Give the extent of all Plasmodium falciparum-infected red blood cells.
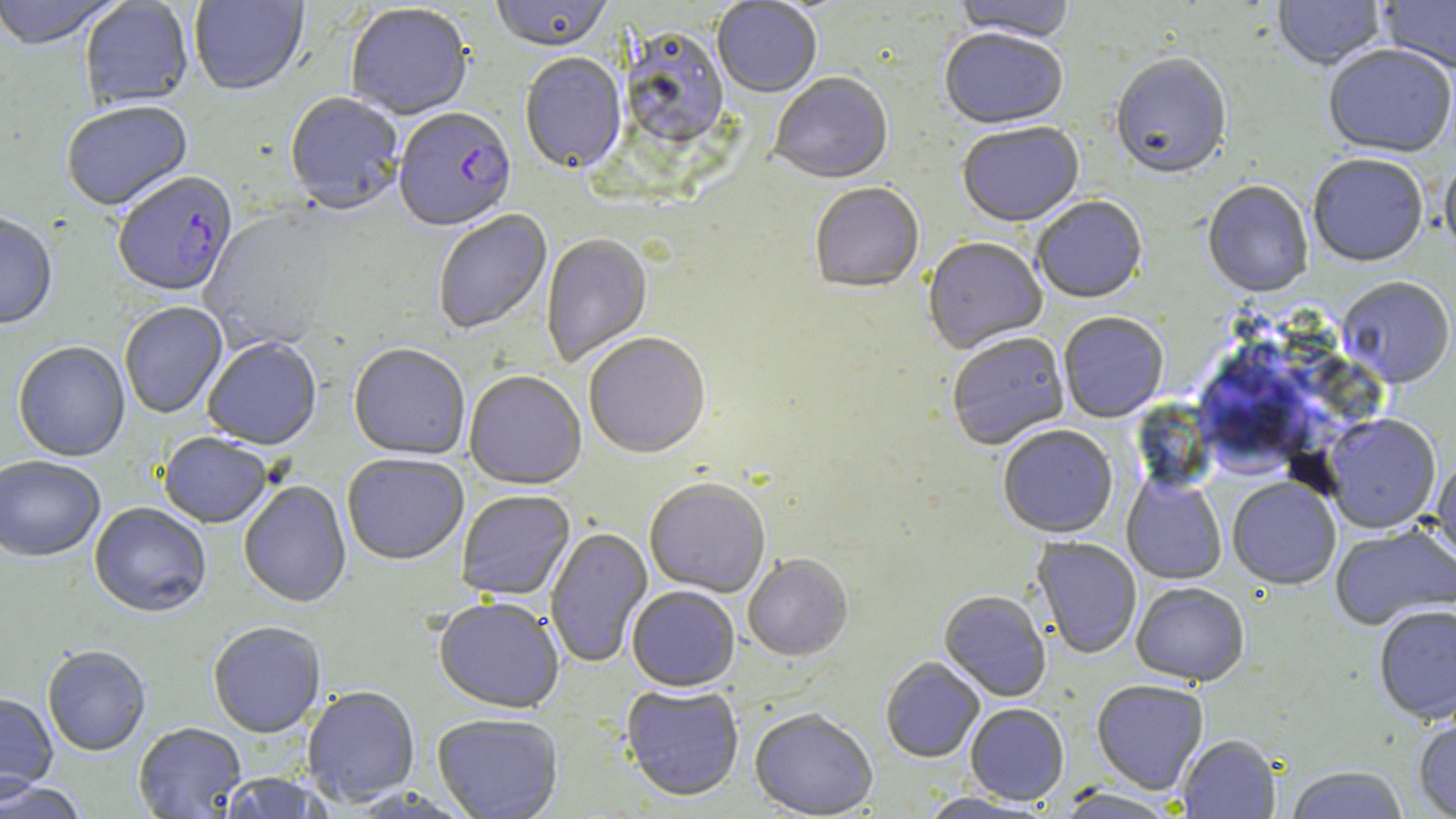

Approximate bounding boxes as (x1,y1)-(x2,y2) corner pairs in pixels.
Plasmodium falciparum-infected red blood cells: (393,109)-(517,234), (113,174)-(238,299).

slide_level_diagnosis: Plasmodium falciparum
field_of_view: single
modality: light microscopy
magnification: 1000x
stain: May-Grünwald-Giemsa
uninfected_red_blood_cell_locations: 'approximate bounding boxes as (x1,y1)-(x2,y2) corner pairs in pixels: (0,0)-(122,53), (79,0)-(194,111), (189,0)-(309,98), (490,0)-(614,54), (1273,0)-(1386,72), (1379,0)-(1456,76), (712,1)-(822,99), (952,1)-(1076,45), (346,5)-(473,122), (620,30)-(731,151), (939,30)-(1068,133), (1323,46)-(1455,159), (519,54)-(627,176), (1110,56)-(1232,183), (769,74)-(894,187), (284,94)-(404,216), (61,103)-(193,214), (957,124)-(1084,229), (1308,155)-(1429,267), (1440,159)-(1456,264), (1203,182)-(1313,298), (810,184)-(924,295), (1032,198)-(1147,305), (434,210)-(553,335), (0,215)-(57,332), (541,234)-(653,368), (923,239)-(1047,355), (1337,277)-(1455,388), (120,303)-(228,420), (1059,313)-(1168,423), (948,334)-(1070,452), (584,335)-(711,461), (203,339)-(322,451), (13,343)-(130,462), (348,345)-(470,462), (1194,353)-(1305,472), (464,373)-(586,491), (1323,414)-(1441,534), (998,425)-(1118,539), (159,435)-(272,529), (342,456)-(469,567), (1431,456)-(1456,566), (0,458)-(105,564), (1122,473)-(1227,584), (1227,478)-(1341,590), (644,480)-(771,599), (239,481)-(352,610), (456,491)-(575,602), (89,504)-(211,619), (1329,523)-(1456,630), (545,528)-(653,668), (1032,537)-(1142,659), (743,555)-(853,663), (1132,581)-(1249,686), (627,587)-(739,692), (939,591)-(1051,702), (434,599)-(564,715), (1373,605)-(1456,724), (208,623)-(326,739), (42,646)-(151,757), (880,658)-(985,763), (1091,679)-(1209,795), (621,686)-(744,802), (302,687)-(420,807), (0,694)-(59,800), (965,704)-(1069,806), (1413,706)-(1456,819), (749,709)-(878,818), (433,714)-(563,819), (134,724)-(247,818), (1177,735)-(1281,818), (1284,766)-(1409,818), (215,772)-(336,818), (0,779)-(88,819), (1051,788)-(1180,819), (915,792)-(1050,819)'
image_size: 1456×819 pixels
preparation: thin blood smear